Report the malaria status of this cell.
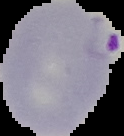
It is parasitized.

preparation = thin blood smear
image size = 124×136 pixels
image type = cell region segmented out of the field of view; surrounding area masked to black